Assess this cell for malaria.
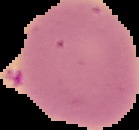
Uninfected.

image type = segmented cell region on a black background
preparation = thin blood film
image size = 139×130 pixels